Report the malaria status of this cell.
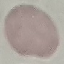

Uninfected.

Summary:
  - Preparation: thin smear
  - Image type: automatically extracted cell patch, resized to 64 × 64 pixels
  - Stain: Giemsa
  - Capture: smartphone camera at the microscope eyepiece